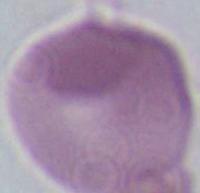
Summary:
  - Identification: erythrocyte
  - Modality: photomicrograph
  - Magnification: 1000x